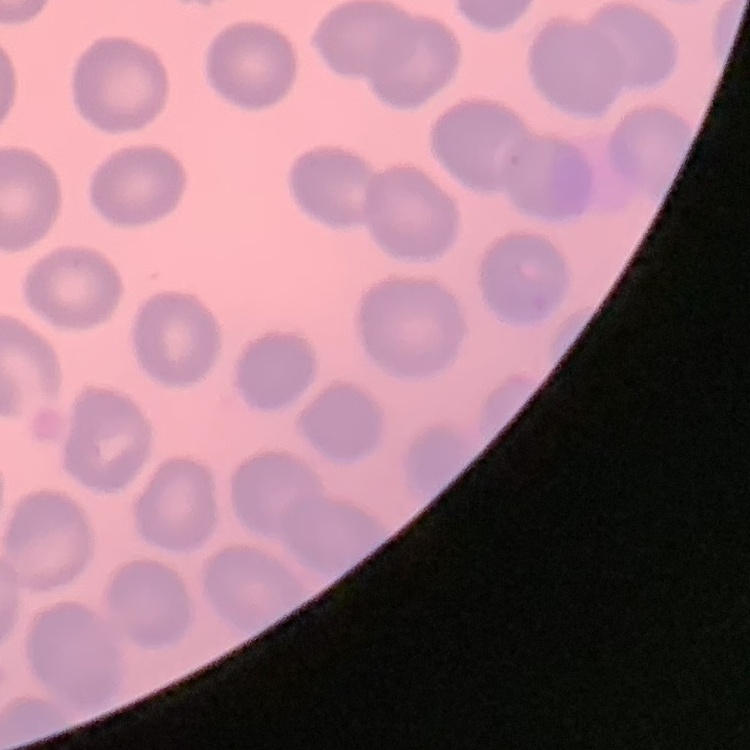

The red blood cells show no rouleaux formation. Thin blood film. Square crop of a larger photomicrograph. Field's or Giemsa stain.